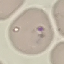

result = no malaria parasites detected
preparation = thin smear
image type = cell patch, automatically extracted from a larger field of view and resized to 64 × 64 pixels
stain = Giemsa
capture = smartphone camera at the microscope eyepiece